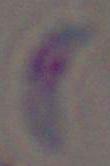

magnification = 1000x
modality = photomicrograph
identification = Toxoplasma gondii